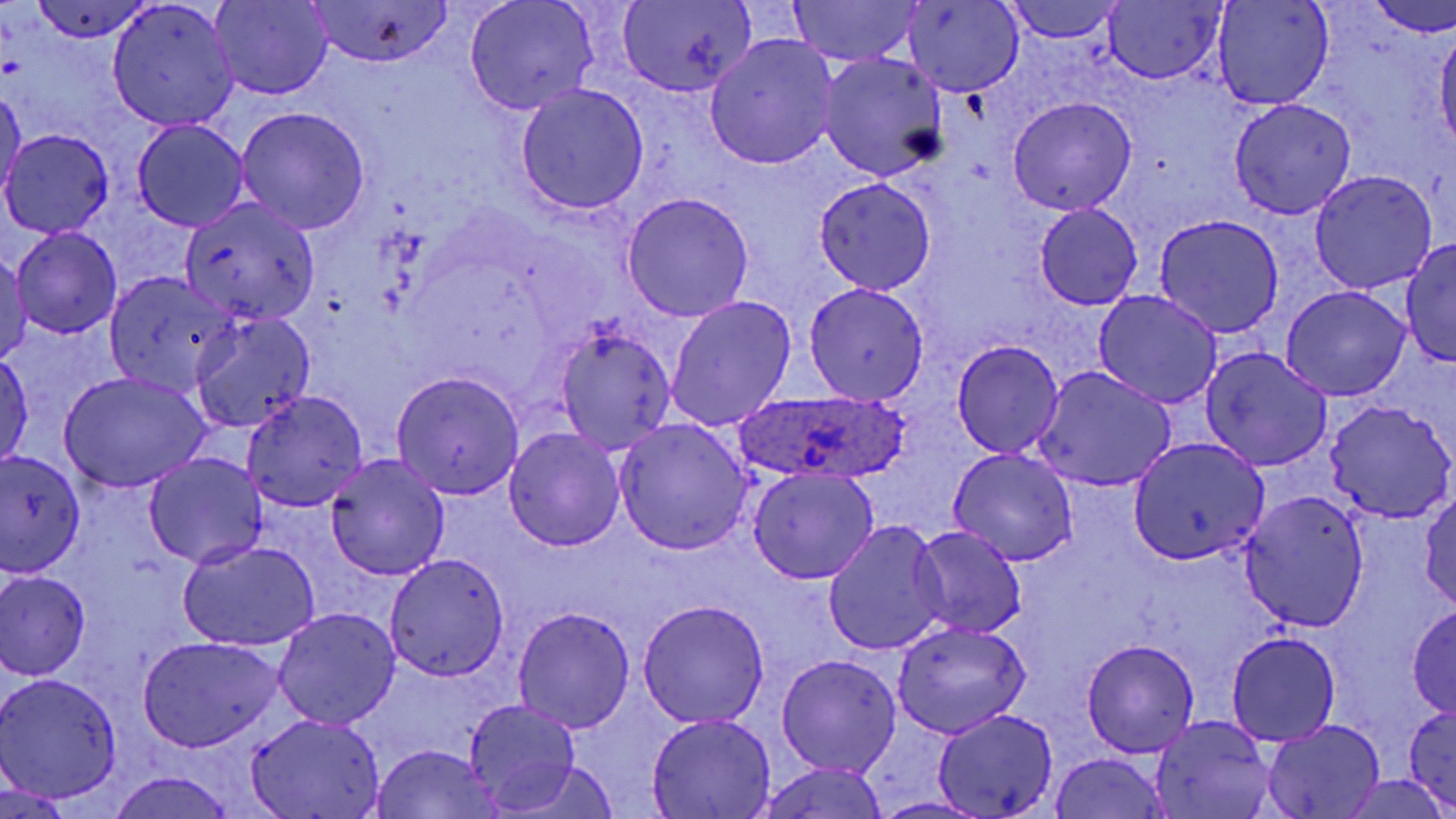

slide-level diagnosis = Plasmodium ovale
stain = May-Grünwald-Giemsa
magnification = 1000x
uninfected red blood cell locations = approximate bounding boxes as named x1/y1/x2/y2 corners in pixels: (x1=211, y1=0, x2=331, y2=100), (x1=789, y1=0, x2=922, y2=67), (x1=901, y1=0, x2=1022, y2=98), (x1=1211, y1=0, x2=1333, y2=110), (x1=1367, y1=0, x2=1456, y2=37), (x1=31, y1=1, x2=154, y2=43), (x1=466, y1=1, x2=598, y2=115), (x1=1002, y1=1, x2=1123, y2=45), (x1=617, y1=2, x2=755, y2=97), (x1=1101, y1=2, x2=1226, y2=84), (x1=106, y1=3, x2=240, y2=132), (x1=304, y1=3, x2=456, y2=69), (x1=1436, y1=24, x2=1456, y2=151), (x1=706, y1=35, x2=839, y2=169), (x1=817, y1=52, x2=948, y2=179), (x1=515, y1=84, x2=648, y2=216), (x1=0, y1=86, x2=26, y2=203), (x1=1009, y1=97, x2=1137, y2=217), (x1=1229, y1=98, x2=1357, y2=220), (x1=234, y1=107, x2=371, y2=234), (x1=131, y1=120, x2=250, y2=233), (x1=2, y1=130, x2=113, y2=237), (x1=1308, y1=170, x2=1439, y2=294), (x1=814, y1=178, x2=935, y2=295), (x1=622, y1=192, x2=754, y2=322), (x1=179, y1=197, x2=323, y2=325), (x1=1034, y1=205, x2=1143, y2=309), (x1=1155, y1=214, x2=1284, y2=338), (x1=12, y1=227, x2=123, y2=339), (x1=1401, y1=237, x2=1456, y2=368), (x1=1, y1=252, x2=33, y2=362), (x1=106, y1=273, x2=241, y2=395), (x1=803, y1=283, x2=930, y2=406), (x1=1283, y1=286, x2=1409, y2=401), (x1=1094, y1=290, x2=1221, y2=409), (x1=666, y1=296, x2=797, y2=430), (x1=188, y1=310, x2=316, y2=434), (x1=553, y1=326, x2=676, y2=454), (x1=952, y1=340, x2=1065, y2=457), (x1=1201, y1=346, x2=1332, y2=472), (x1=1, y1=352, x2=34, y2=471), (x1=1032, y1=366, x2=1176, y2=491), (x1=391, y1=370, x2=525, y2=499), (x1=59, y1=373, x2=211, y2=493), (x1=240, y1=390, x2=370, y2=512), (x1=1323, y1=400, x2=1456, y2=525), (x1=614, y1=419, x2=752, y2=555), (x1=503, y1=427, x2=626, y2=552), (x1=1126, y1=438, x2=1271, y2=565), (x1=947, y1=447, x2=1078, y2=566), (x1=1, y1=452, x2=87, y2=574), (x1=143, y1=452, x2=268, y2=568), (x1=325, y1=454, x2=450, y2=581), (x1=747, y1=468, x2=877, y2=583), (x1=1237, y1=491, x2=1370, y2=630), (x1=758, y1=492, x2=938, y2=629), (x1=1418, y1=493, x2=1456, y2=610), (x1=822, y1=520, x2=950, y2=656), (x1=910, y1=526, x2=1027, y2=640), (x1=177, y1=540, x2=320, y2=652), (x1=383, y1=552, x2=510, y2=681), (x1=0, y1=571, x2=91, y2=678), (x1=636, y1=600, x2=768, y2=726), (x1=512, y1=605, x2=635, y2=734), (x1=1407, y1=605, x2=1456, y2=718), (x1=272, y1=608, x2=401, y2=729), (x1=891, y1=619, x2=1033, y2=739), (x1=1227, y1=632, x2=1339, y2=745), (x1=138, y1=635, x2=283, y2=753), (x1=1081, y1=639, x2=1199, y2=758), (x1=777, y1=654, x2=901, y2=777), (x1=1, y1=672, x2=124, y2=802), (x1=462, y1=700, x2=580, y2=814), (x1=1403, y1=706, x2=1456, y2=809), (x1=933, y1=708, x2=1059, y2=817), (x1=247, y1=712, x2=386, y2=818), (x1=646, y1=714, x2=778, y2=817), (x1=1150, y1=716, x2=1277, y2=818), (x1=1263, y1=721, x2=1386, y2=818), (x1=370, y1=744, x2=505, y2=818), (x1=1047, y1=752, x2=1172, y2=819), (x1=499, y1=761, x2=622, y2=819), (x1=758, y1=763, x2=890, y2=819), (x1=108, y1=770, x2=236, y2=819), (x1=1341, y1=774, x2=1451, y2=819), (x1=872, y1=796, x2=987, y2=818)
Plasmodium ovale-infected red blood cell locations = approximate bounding boxes as named x1/y1/x2/y2 corners in pixels: (x1=731, y1=390, x2=914, y2=487)
modality = light microscopy
field of view = single
image size = 1456×819 pixels
preparation = thin blood film